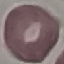

result = no malaria parasites seen
stain = Giemsa
preparation = thin blood film
capture = smartphone through the microscope eyepiece
image type = automatically extracted cell patch, resized to 64 × 64 pixels